Mark where platelets are.
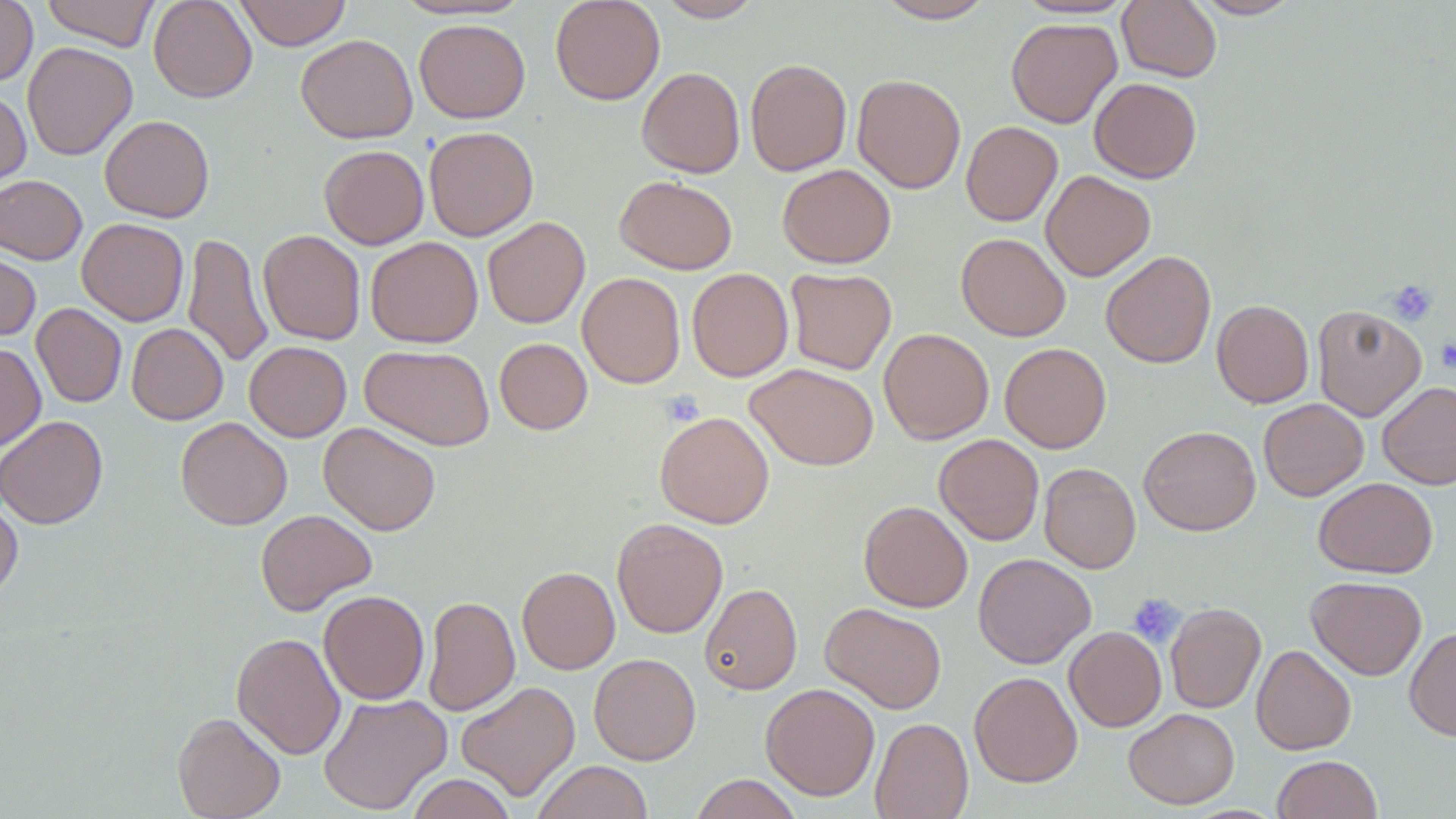

Approximate bounding boxes as (x1,y1)-(x2,y2) corner pairs in pixels.
Platelets: (1387,279)-(1437,326), (1436,338)-(1456,372), (661,390)-(704,427), (1127,593)-(1184,646).

Uninfected red blood cell locations: (0,0)-(38,86), (41,0)-(161,51), (148,0)-(257,103), (234,0)-(351,50), (391,0)-(532,21), (550,0)-(665,105), (655,0)-(765,22), (1015,0)-(1136,20), (1190,0)-(1301,19), (874,1)-(996,23), (1118,1)-(1222,82), (1006,17)-(1122,128), (414,18)-(530,123), (295,34)-(418,143), (22,42)-(138,160), (745,59)-(852,176), (637,67)-(745,178), (852,74)-(966,194), (1089,78)-(1202,183), (0,89)-(31,191), (100,115)-(214,222), (961,121)-(1062,226), (424,126)-(538,241), (319,145)-(429,249), (777,164)-(896,268), (1041,170)-(1155,281), (0,175)-(87,264), (615,175)-(737,274), (482,217)-(590,329), (77,218)-(189,326), (259,229)-(365,345), (183,232)-(273,370), (956,233)-(1071,341), (366,236)-(483,348), (0,247)-(41,342), (1101,250)-(1216,368), (687,267)-(793,382), (785,268)-(896,375), (577,272)-(685,389), (1212,299)-(1314,408), (31,303)-(127,408), (1312,304)-(1427,421), (126,323)-(228,425), (879,328)-(994,444), (494,338)-(592,435), (244,341)-(351,442), (0,343)-(46,452), (999,343)-(1111,453), (360,344)-(495,451), (745,363)-(879,471), (1376,381)-(1456,490), (1258,398)-(1369,501), (654,411)-(774,528), (0,415)-(108,529), (175,417)-(292,530), (318,422)-(441,535), (1138,425)-(1261,535), (934,433)-(1044,545), (1039,462)-(1140,573), (1314,477)-(1438,578), (0,499)-(23,600), (859,501)-(972,612), (255,509)-(376,615), (612,518)-(728,638), (973,553)-(1096,669), (517,566)-(620,674), (1306,575)-(1427,680), (700,583)-(802,695), (319,590)-(429,704), (422,595)-(520,716), (820,602)-(947,714), (1165,602)-(1265,713), (1064,626)-(1166,732), (1405,626)-(1456,741), (232,632)-(346,760), (1252,645)-(1356,755), (589,653)-(701,765), (969,671)-(1082,787), (456,681)-(580,801), (760,682)-(880,801), (317,692)-(452,815), (1124,708)-(1240,809), (173,712)-(285,819), (870,717)-(973,819), (1272,754)-(1382,819), (533,760)-(653,819), (407,773)-(516,819), (690,774)-(802,819). Slide-level diagnosis: negative for blood parasites. Optical microscopy. May-Grünwald-Giemsa-stained preparation. Captured at 1000x magnification. One field of a larger specimen. Image is 1456×819 pixels. Thin blood film.